Identify the cell.
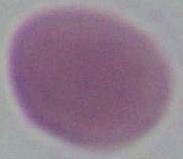
An erythrocyte.

Captured at 1000x magnification. Micrograph.